Assess this cell for malaria.
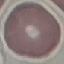
It is uninfected.

Automatically extracted cell patch, resized to 64 × 64 pixels. Thin smear of blood. Giemsa-stained preparation. Photographed with a smartphone camera at the microscope eyepiece.